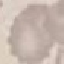
malaria_status: uninfected
image_type: automatically extracted cell patch, resized to 64 × 64 pixels
stain: Giemsa
preparation: thin blood smear
capture: smartphone camera at the microscope eyepiece